Look for Plasmodium parasites.
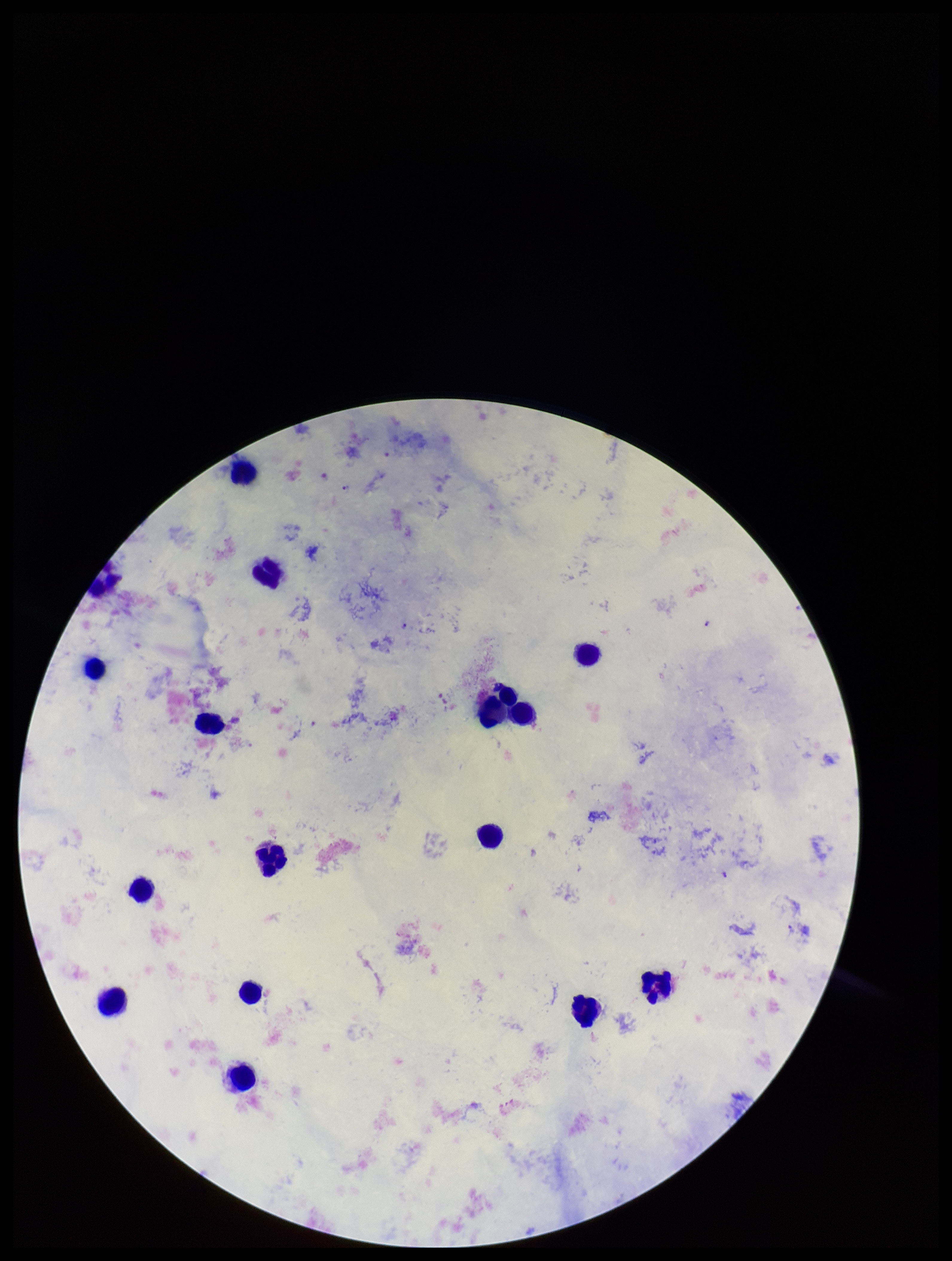

Detected.

Patient malaria status: infected. One field from this slide. Giemsa stain. Species reported for this patient: Plasmodium falciparum. Image is 952×1261 pixels. Parasite count: 4. Leukocyte count: 16. Preparation: thick smear. Photographed through the microscope eyepiece with a smartphone camera.